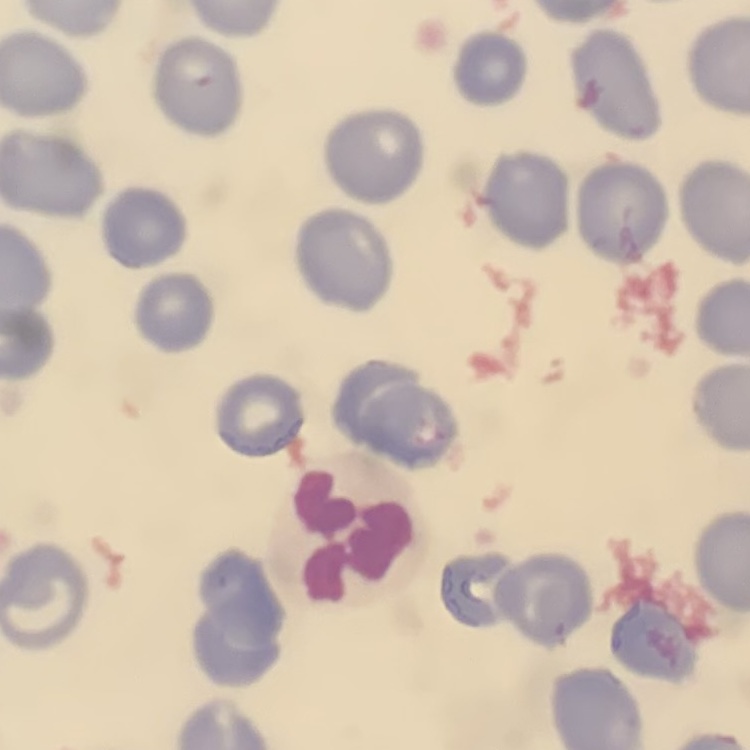

Summary:
  - Erythrocyte morphology: no rouleaux formation
  - Stain: Field's or Giemsa
  - Image type: square crop of a larger photomicrograph
  - Preparation: thin blood smear